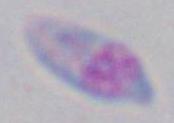
Photomicrograph. Captured at 1000x magnification. Toxoplasma gondii is shown.